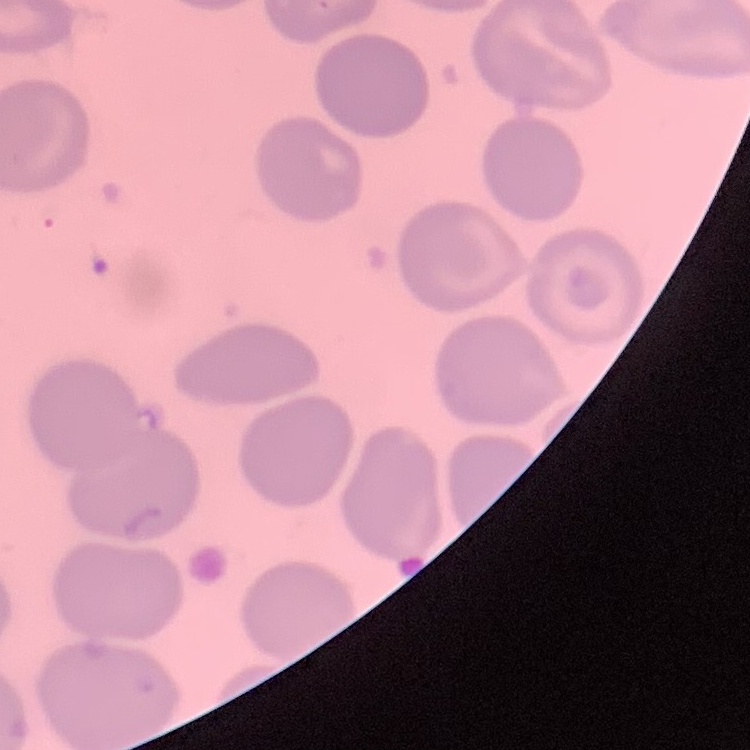

The erythrocytes show no rouleaux formation. Stained with either Field's or Giemsa. Square crop of a larger photomicrograph. Thin blood smear.